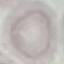

Summary:
  - Malaria status: uninfected
  - Stain: Giemsa
  - Preparation: thin blood film
  - Capture: smartphone through the microscope eyepiece
  - Image type: automatically extracted cell patch, resized to 64 × 64 pixels